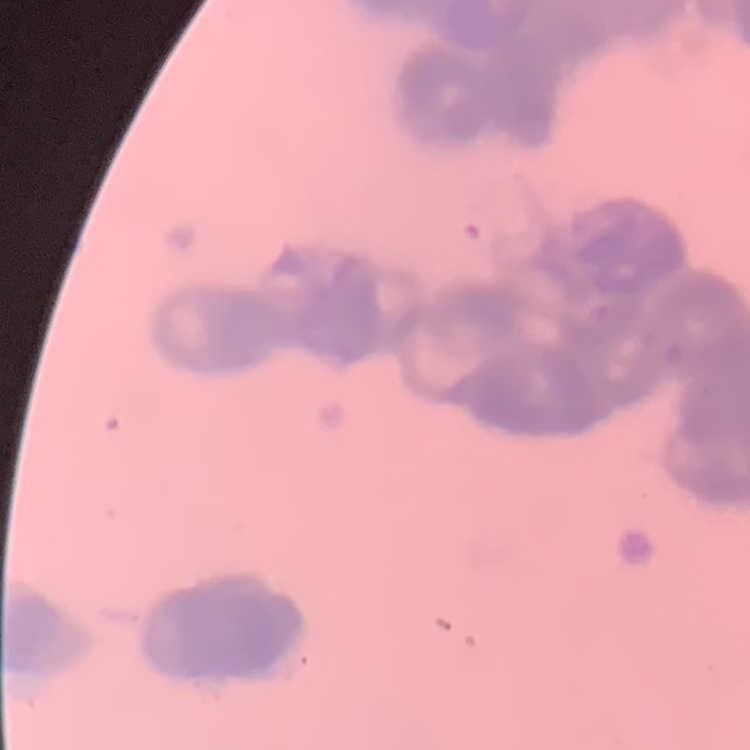
erythrocyte morphology = rouleaux formation
preparation = thin blood smear
image type = one tile cut from a larger photomicrograph
stain = Field's or Giemsa